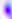

{
  "magnification": "400x",
  "modality": "micrograph",
  "identification": "Toxoplasma gondii"
}